Assess the morphology of the red blood cells.
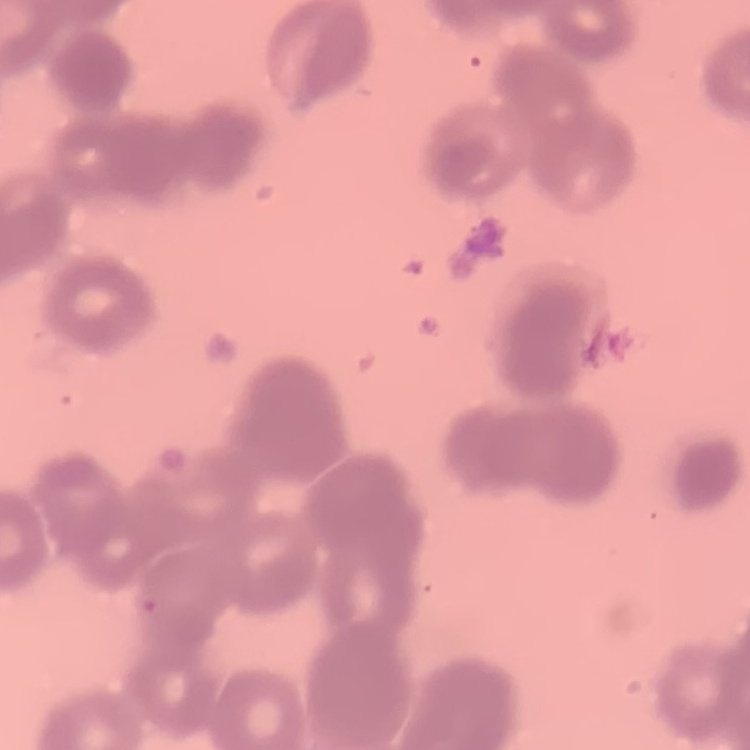

They show rouleaux formation.

Summary:
  - Image type: one tile cut from a larger photomicrograph
  - Preparation: thin blood smear
  - Stain: Field's or Giemsa